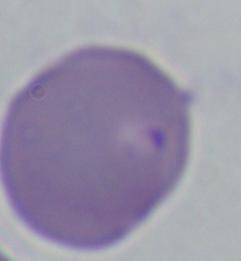
A Babesia parasite is shown. 1000x magnification. Photomicrograph.